Locate every Plasmodium parasite.
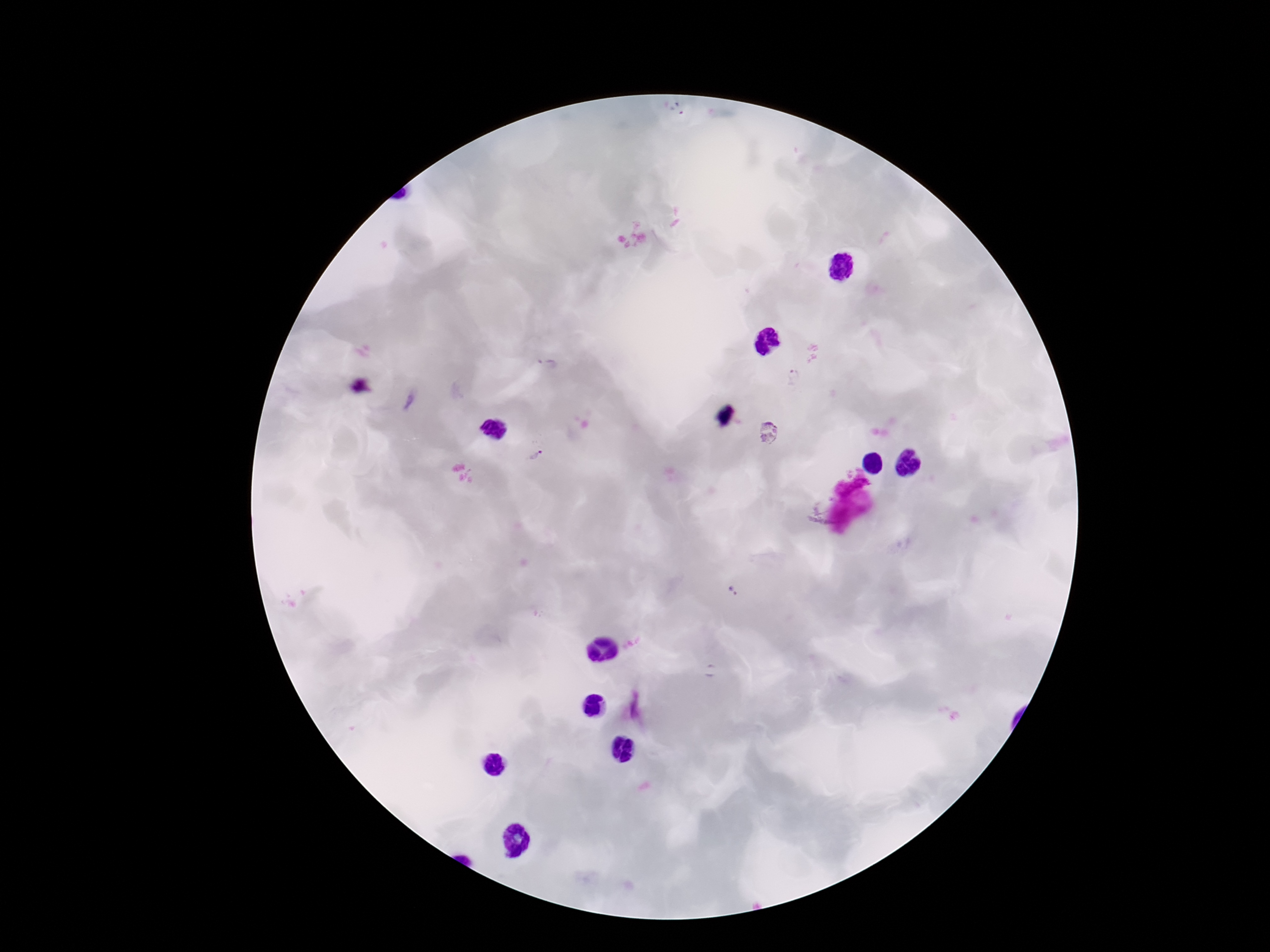

Approximate centers as (x, y) in pixels.
Plasmodium parasites: (548, 364), (795, 376), (769, 434), (535, 455), (732, 591).

image size = 1270×952 pixels
stain = Giemsa
preparation = thick peripheral-blood smear
field of view = one from this slide
patient malaria status = infected
capture = smartphone camera through the microscope eyepiece
magnification = 100x